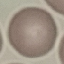

malaria_status: uninfected
stain: Giemsa
image_type: automatically extracted cell patch, resized to 64 × 64 pixels
capture: smartphone through the microscope eyepiece
preparation: thin blood smear